Name the blood parasite species.
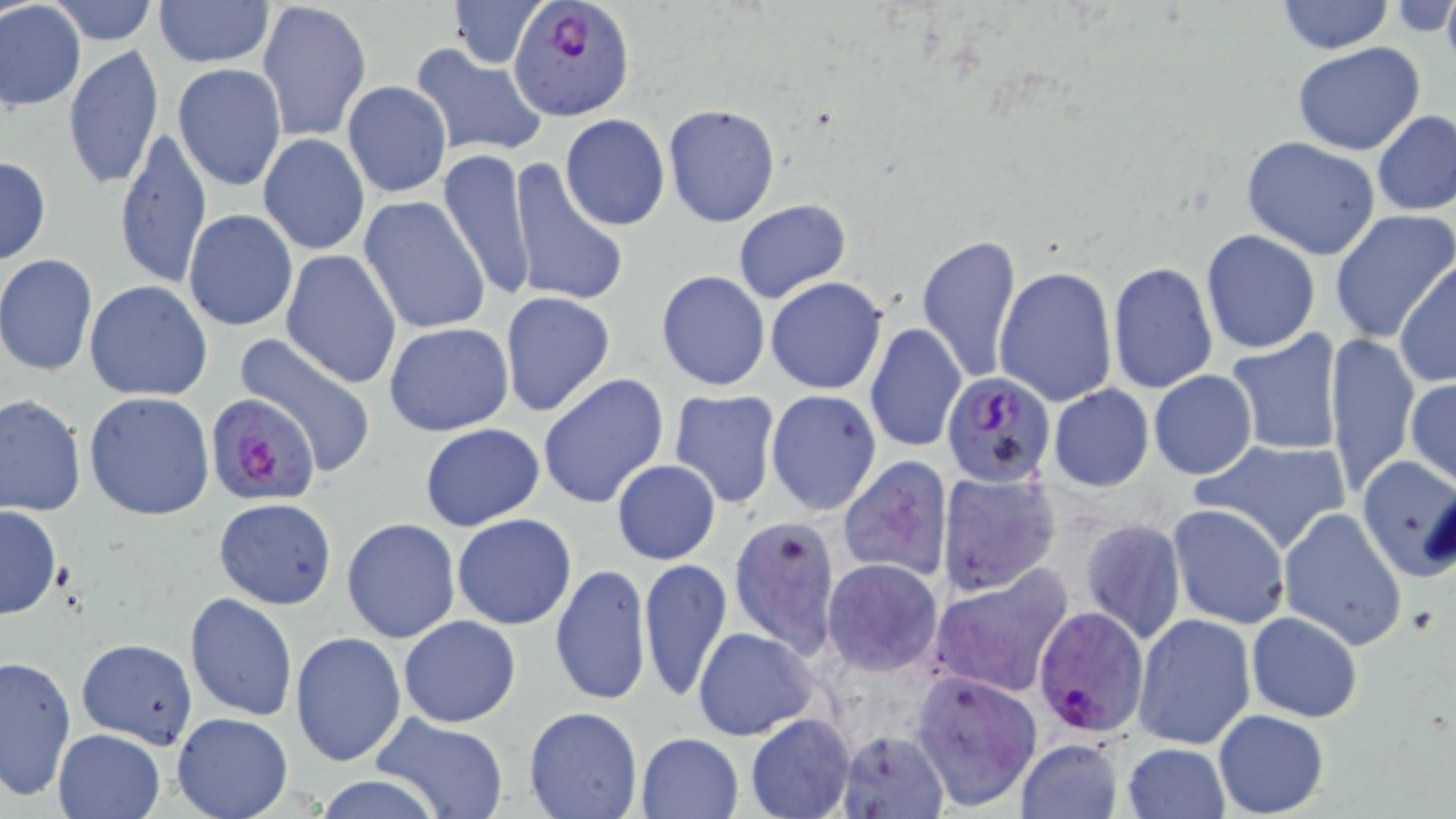

Plasmodium falciparum.

{
  "uninfected_red_blood_cell_locations": "approximate bounding boxes as named x1/y1/x2/y2 corners in pixels: (x1=45, y1=0, x2=160, y2=46), (x1=448, y1=0, x2=545, y2=69), (x1=1275, y1=0, x2=1394, y2=54), (x1=151, y1=1, x2=274, y2=68), (x1=258, y1=1, x2=370, y2=142), (x1=1388, y1=1, x2=1456, y2=39), (x1=0, y1=2, x2=86, y2=111), (x1=1292, y1=43, x2=1425, y2=155), (x1=63, y1=44, x2=164, y2=190), (x1=409, y1=44, x2=547, y2=160), (x1=172, y1=62, x2=286, y2=193), (x1=342, y1=81, x2=451, y2=198), (x1=662, y1=103, x2=782, y2=229), (x1=1372, y1=110, x2=1456, y2=217), (x1=560, y1=114, x2=670, y2=231), (x1=114, y1=126, x2=211, y2=291), (x1=260, y1=133, x2=368, y2=254), (x1=1241, y1=135, x2=1384, y2=260), (x1=438, y1=148, x2=537, y2=305), (x1=0, y1=155, x2=51, y2=267), (x1=509, y1=158, x2=629, y2=310), (x1=360, y1=195, x2=490, y2=335), (x1=732, y1=198, x2=850, y2=303), (x1=1328, y1=209, x2=1456, y2=342), (x1=182, y1=210, x2=297, y2=332), (x1=1200, y1=228, x2=1321, y2=354), (x1=916, y1=232, x2=1023, y2=383), (x1=280, y1=250, x2=400, y2=389), (x1=0, y1=254, x2=98, y2=377), (x1=1394, y1=259, x2=1455, y2=387), (x1=1106, y1=260, x2=1218, y2=396), (x1=992, y1=264, x2=1118, y2=407), (x1=655, y1=270, x2=771, y2=392), (x1=764, y1=276, x2=889, y2=394), (x1=84, y1=280, x2=214, y2=401), (x1=499, y1=292, x2=616, y2=418), (x1=384, y1=321, x2=513, y2=437), (x1=865, y1=322, x2=967, y2=453), (x1=1225, y1=328, x2=1345, y2=457), (x1=234, y1=331, x2=377, y2=477), (x1=1324, y1=332, x2=1419, y2=494), (x1=1148, y1=370, x2=1257, y2=480), (x1=538, y1=372, x2=670, y2=509), (x1=1405, y1=377, x2=1456, y2=490), (x1=1046, y1=383, x2=1155, y2=493), (x1=667, y1=389, x2=781, y2=509), (x1=766, y1=390, x2=881, y2=515), (x1=84, y1=391, x2=215, y2=521), (x1=1, y1=395, x2=86, y2=515), (x1=419, y1=422, x2=544, y2=531), (x1=1191, y1=437, x2=1353, y2=554), (x1=1354, y1=454, x2=1456, y2=581), (x1=837, y1=456, x2=954, y2=581), (x1=612, y1=459, x2=720, y2=564), (x1=936, y1=469, x2=1061, y2=594), (x1=213, y1=497, x2=338, y2=609), (x1=1168, y1=504, x2=1290, y2=629), (x1=0, y1=505, x2=62, y2=619), (x1=1278, y1=508, x2=1408, y2=651), (x1=452, y1=513, x2=578, y2=630), (x1=731, y1=516, x2=841, y2=658), (x1=342, y1=517, x2=461, y2=644), (x1=1079, y1=517, x2=1186, y2=645), (x1=638, y1=558, x2=732, y2=702), (x1=822, y1=559, x2=944, y2=677), (x1=549, y1=563, x2=650, y2=709), (x1=930, y1=567, x2=1074, y2=697), (x1=184, y1=592, x2=298, y2=721), (x1=1133, y1=612, x2=1256, y2=748), (x1=1246, y1=612, x2=1362, y2=723), (x1=398, y1=615, x2=520, y2=727), (x1=296, y1=624, x2=521, y2=743), (x1=693, y1=628, x2=817, y2=741), (x1=290, y1=632, x2=407, y2=767), (x1=77, y1=637, x2=200, y2=747), (x1=0, y1=653, x2=76, y2=801), (x1=908, y1=668, x2=1042, y2=812), (x1=524, y1=706, x2=643, y2=819), (x1=1214, y1=710, x2=1328, y2=817), (x1=171, y1=713, x2=292, y2=819), (x1=746, y1=714, x2=856, y2=819), (x1=369, y1=715, x2=511, y2=819), (x1=54, y1=729, x2=165, y2=818), (x1=837, y1=729, x2=948, y2=818), (x1=636, y1=732, x2=743, y2=818), (x1=1014, y1=738, x2=1122, y2=819), (x1=1121, y1=742, x2=1230, y2=819), (x1=310, y1=776, x2=448, y2=817)",
  "magnification": "1000x",
  "plasmodium_falciparum_infected_red_blood_cell_locations": "approximate bounding boxes as named x1/y1/x2/y2 corners in pixels: (x1=508, y1=0, x2=636, y2=120), (x1=940, y1=375, x2=1055, y2=487), (x1=207, y1=395, x2=322, y2=506), (x1=1033, y1=607, x2=1148, y2=738)",
  "modality": "optical microscopy",
  "image_size": "1456×819 pixels",
  "field_of_view": "single",
  "preparation": "thin blood film",
  "stain": "May-Grünwald-Giemsa"
}